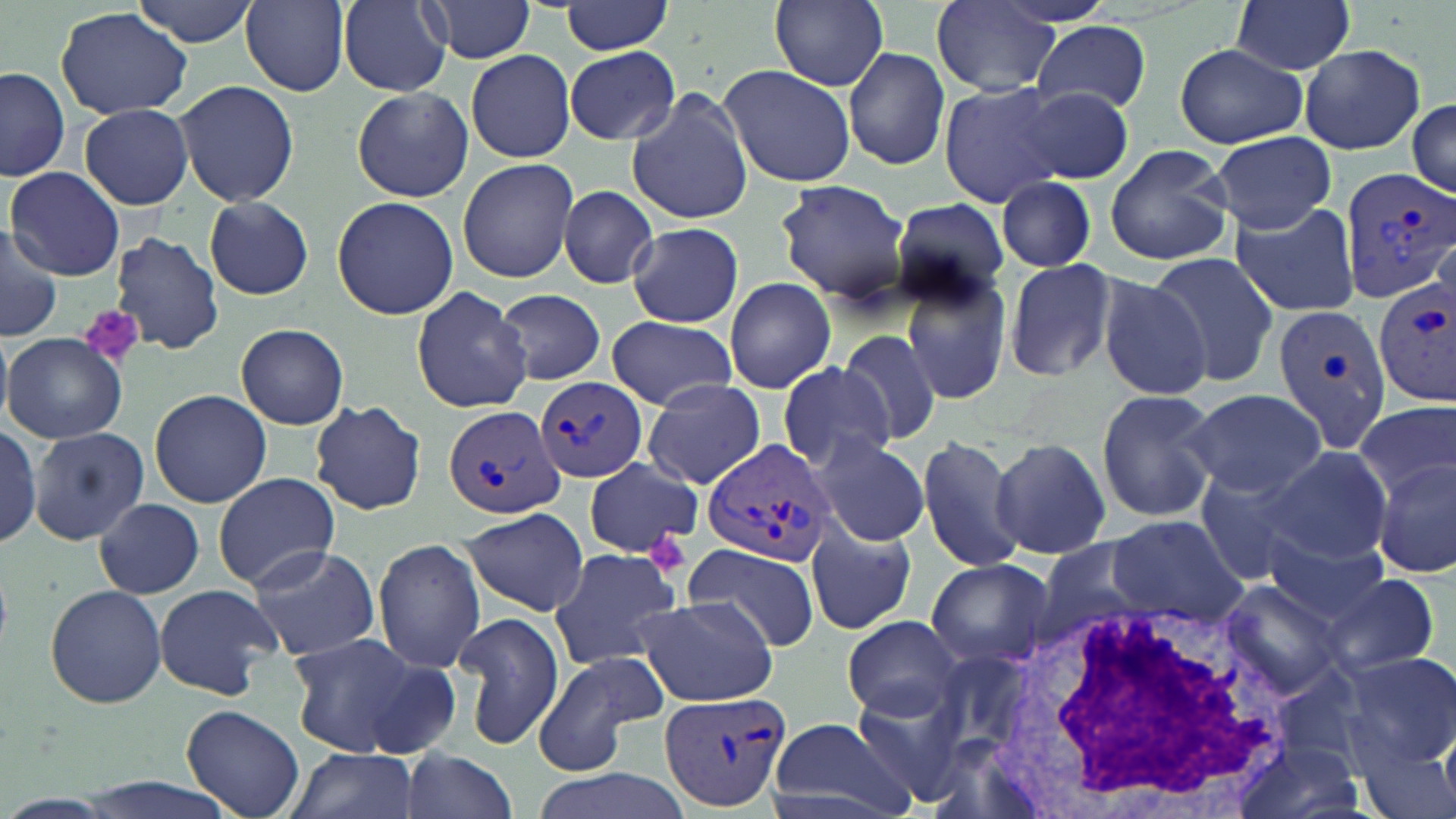

{
  "slide_level_diagnosis": "Plasmodium vivax",
  "image_size": "1456×819 pixels",
  "uninfected_red_blood_cell_locations": "approximate bounding boxes as (x1,y1)-(x2,y2) corner pairs in pixels: (132,0)-(260,46), (421,0)-(538,67), (770,0)-(889,90), (1231,0)-(1358,77), (241,1)-(351,95), (337,2)-(453,95), (562,2)-(676,54), (931,2)-(1059,95), (55,7)-(192,120), (1034,21)-(1152,113), (1174,43)-(1308,148), (1298,45)-(1425,155), (564,46)-(680,143), (843,47)-(951,171), (465,49)-(576,163), (720,64)-(856,187), (0,68)-(71,179), (175,77)-(300,209), (937,80)-(1066,208), (626,86)-(753,223), (1018,86)-(1135,181), (352,87)-(475,203), (1407,99)-(1456,198), (78,103)-(192,209), (1211,131)-(1335,233), (1103,144)-(1235,266), (457,157)-(580,283), (6,167)-(125,279), (995,175)-(1097,273), (775,179)-(915,303), (557,185)-(660,289), (889,195)-(1011,304), (331,196)-(458,319), (204,197)-(313,300), (1231,205)-(1360,315), (628,221)-(744,328), (0,225)-(64,341), (111,229)-(224,355), (1149,252)-(1280,388), (1002,256)-(1123,385), (901,264)-(1015,405), (1097,275)-(1213,400), (723,278)-(836,392), (411,286)-(532,413), (494,289)-(610,384), (608,315)-(735,409), (234,325)-(353,430), (837,328)-(941,448), (4,332)-(126,443), (775,360)-(895,473), (642,379)-(766,490), (149,388)-(272,508), (1095,388)-(1220,525), (1185,389)-(1327,498), (309,399)-(427,515), (1355,401)-(1455,499), (0,427)-(43,547), (30,429)-(150,543), (811,434)-(930,547), (915,434)-(1025,574), (989,437)-(1109,560), (1263,444)-(1391,563), (1373,458)-(1456,577), (584,459)-(702,557), (1194,466)-(1316,585), (213,472)-(341,590), (95,497)-(204,598), (459,506)-(590,617), (1105,516)-(1248,622), (807,522)-(918,634), (1261,526)-(1387,624), (374,537)-(484,675), (246,542)-(380,662), (684,543)-(819,650), (546,546)-(685,671), (925,557)-(1054,669), (1321,573)-(1441,678), (153,582)-(281,699), (1221,582)-(1344,697), (45,583)-(168,709), (636,595)-(779,707), (454,608)-(564,752), (841,615)-(964,719), (283,631)-(435,759), (532,650)-(669,775), (1341,652)-(1456,763), (1273,664)-(1368,777), (182,704)-(304,818), (763,716)-(917,818), (1241,737)-(1366,819), (399,746)-(516,819), (287,747)-(419,819), (528,768)-(695,819)",
  "modality": "light microscopy",
  "field_of_view": "one of a larger specimen",
  "platelet_locations": "approximate bounding boxes as (x1,y1)-(x2,y2) corner pairs in pixels: (82,305)-(145,368), (650,533)-(685,570)",
  "plasmodium_vivax_infected_red_blood_cell_locations": "approximate bounding boxes as (x1,y1)-(x2,y2) corner pairs in pixels: (1336,164)-(1455,303), (1375,281)-(1456,406), (1271,302)-(1394,453), (537,376)-(646,482), (441,404)-(565,519), (700,439)-(838,569), (659,688)-(793,814)",
  "stain": "May-Grünwald-Giemsa",
  "preparation": "thin blood smear",
  "white_blood_cell_locations": "approximate bounding boxes as (x1,y1)-(x2,y2) corner pairs in pixels: (993,597)-(1290,819)",
  "magnification": "1000x"
}